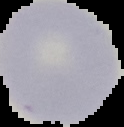

Summary:
  - Result: no Plasmodium parasites seen
  - Preparation: thin blood film
  - Image type: cell region segmented out of the field of view; surrounding area masked to black
  - Image size: 124×127 pixels